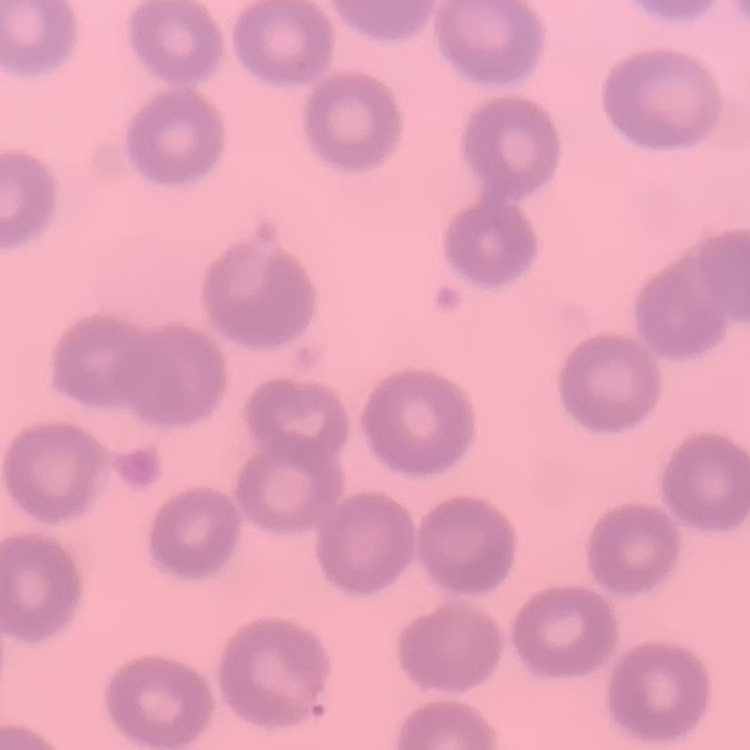

The erythrocytes show no rouleaux formation. Thin blood smear. Stained with either Field's or Giemsa. One tile cut from a larger photomicrograph.